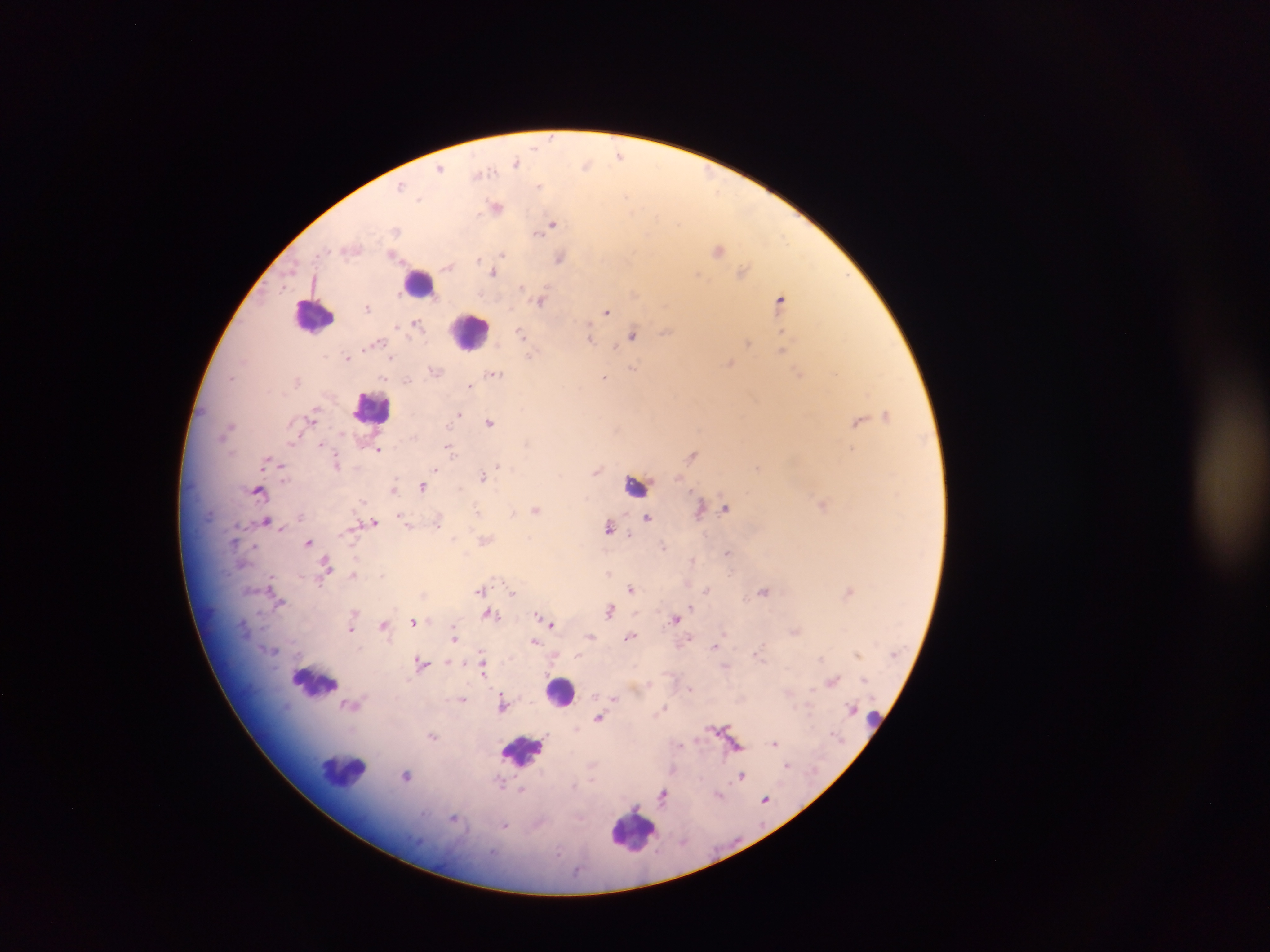
Approximate centers as [x, y] in pixels. Plasmodium parasite locations: [552, 138], [619, 155], [516, 161], [586, 164], [440, 168], [481, 174], [539, 185], [402, 187], [627, 196], [419, 199], [497, 207], [553, 224], [395, 230], [536, 232], [352, 248], [718, 249], [503, 254], [394, 256], [478, 257], [560, 258], [448, 265], [743, 271], [494, 273], [697, 274], [285, 287], [522, 287], [779, 298], [540, 300], [367, 307], [607, 311], [416, 324], [397, 326], [666, 332], [521, 333], [633, 335], [589, 336], [375, 343], [748, 343], [615, 345], [782, 349], [531, 355], [347, 357], [391, 358], [729, 363], [633, 367], [434, 371], [800, 372], [494, 374], [603, 377], [231, 378], [407, 381], [470, 385], [459, 414], [887, 415], [312, 417], [858, 421], [490, 422], [228, 426], [292, 441], [321, 444], [447, 448], [378, 449], [692, 454], [267, 461], [336, 462], [282, 467], [498, 467], [757, 467], [435, 469], [596, 471], [483, 476], [422, 487], [393, 489], [259, 490], [824, 505], [726, 507], [477, 509], [536, 509], [699, 510], [513, 513], [647, 518], [266, 520], [374, 521], [438, 521], [407, 523], [609, 527], [629, 535], [454, 538], [485, 540], [309, 542], [663, 548], [728, 552], [692, 560], [326, 562], [352, 574], [609, 574], [381, 575], [270, 582], [320, 582], [631, 589], [479, 590], [707, 590], [764, 591], [849, 591], [512, 592], [280, 601], [691, 606], [610, 611], [354, 612], [490, 615], [538, 615], [498, 616], [675, 619], [546, 620], [414, 621], [551, 624], [383, 625], [351, 629], [794, 632], [454, 637], [630, 637], [689, 637], [534, 641], [715, 647], [758, 652], [858, 654], [577, 655], [421, 662], [483, 667], [864, 679], [832, 681], [690, 689], [615, 698], [462, 699], [351, 704], [503, 705], [665, 707], [852, 708], [599, 718], [432, 736], [775, 743], [679, 745], [786, 764], [407, 775], [741, 775], [521, 790], [719, 794], [663, 795], [765, 798], [454, 819], [506, 825]. Leukocyte locations: [420, 282], [314, 315], [471, 331], [372, 407], [637, 485], [315, 683], [560, 691], [872, 718], [523, 749], [345, 775], [633, 830]. One field of view. Thick blood film. Collected in Ghana. Photographed through a microscope with a mobile-phone camera. Image is 1270×952 pixels.